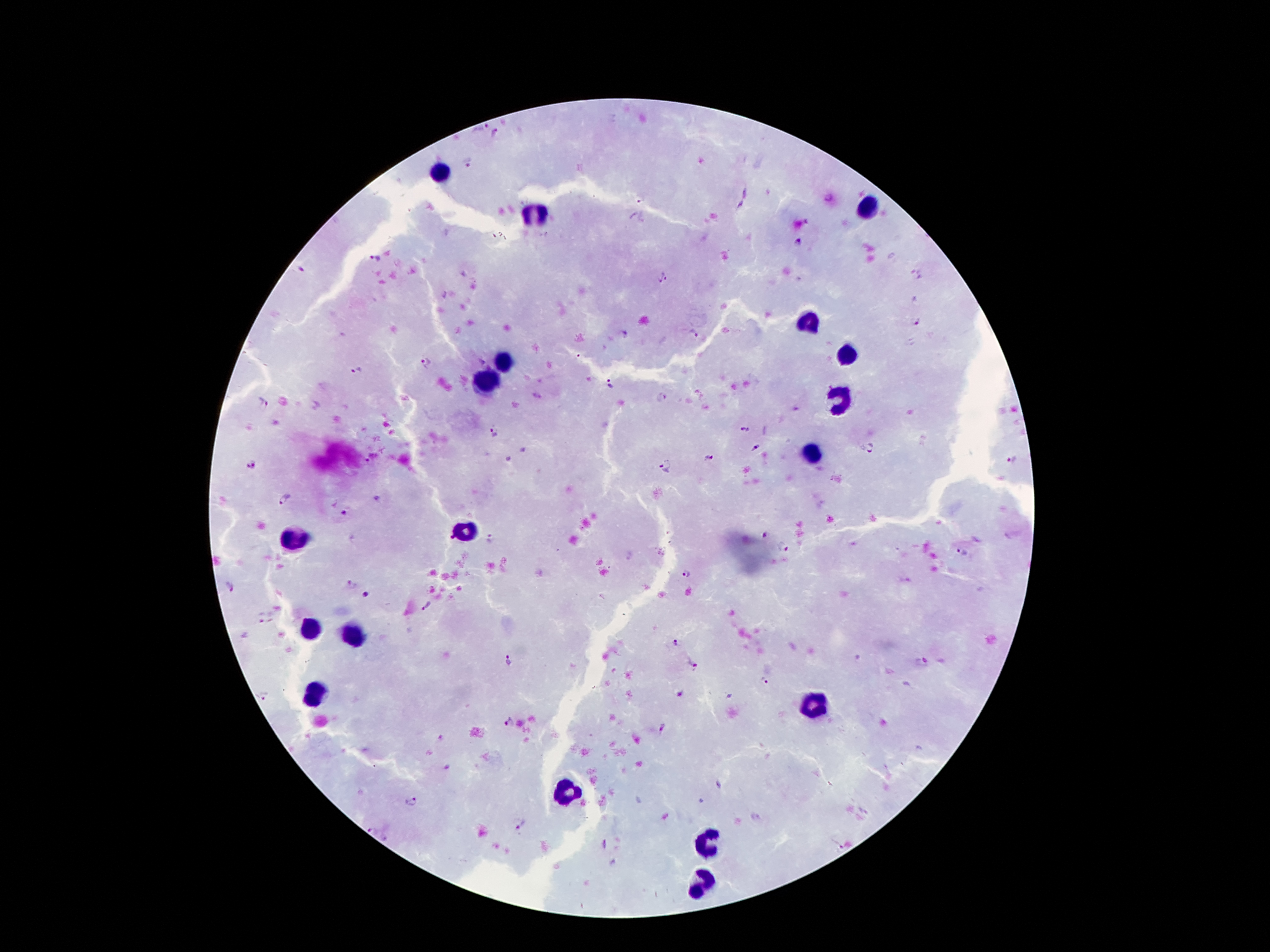 Approximate centers as {x, y} in pixels. Leukocyte locations: {440, 169}, {864, 209}, {539, 214}, {806, 320}, {849, 355}, {503, 359}, {485, 380}, {839, 398}, {815, 451}, {471, 530}, {294, 539}, {311, 628}, {354, 634}, {315, 697}, {816, 701}, {570, 791}, {713, 842}, {704, 881}. Plasmodium parasite locations: {480, 126}, {497, 134}, {469, 166}, {828, 196}, {641, 200}, {797, 243}, {375, 257}, {301, 269}, {916, 275}, {665, 278}, {917, 321}, {695, 334}, {427, 362}, {357, 372}, {611, 383}, {664, 395}, {264, 404}, {744, 429}, {494, 432}, {754, 447}, {871, 449}, {708, 459}, {367, 460}, {1012, 460}, {252, 463}, {667, 467}, {284, 498}, {375, 498}, {344, 513}, {765, 536}, {450, 539}, {491, 540}, {781, 547}, {961, 553}, {683, 573}, {350, 584}, {231, 587}, {365, 593}, {426, 606}, {259, 619}, {674, 644}, {509, 661}, {923, 662}, {696, 668}, {763, 679}, {678, 695}, {266, 696}, {508, 723}, {662, 726}, {441, 740}, {445, 768}, {718, 785}, {411, 801}, {520, 822}, {373, 831}, {603, 844}, {840, 848}. Patient malaria status: positive for Plasmodium falciparum. Image is 1270×952 pixels. Photographed through the microscope eyepiece with a smartphone camera. One field from this slide. 100x magnification. Giemsa-stained preparation. Thick blood smear.